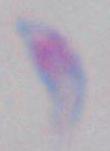
modality = photomicrograph
magnification = 1000x
identification = Toxoplasma gondii